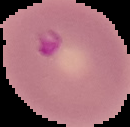 From a thin blood film. Result: Plasmodium parasites detected. Image is 130×127 pixels. Cell region segmented out of the field of view; the surrounding area is masked to black.